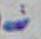

Summary:
  - Magnification: 1000x
  - Identification: Toxoplasma gondii
  - Modality: photomicrograph